Assess for malaria.
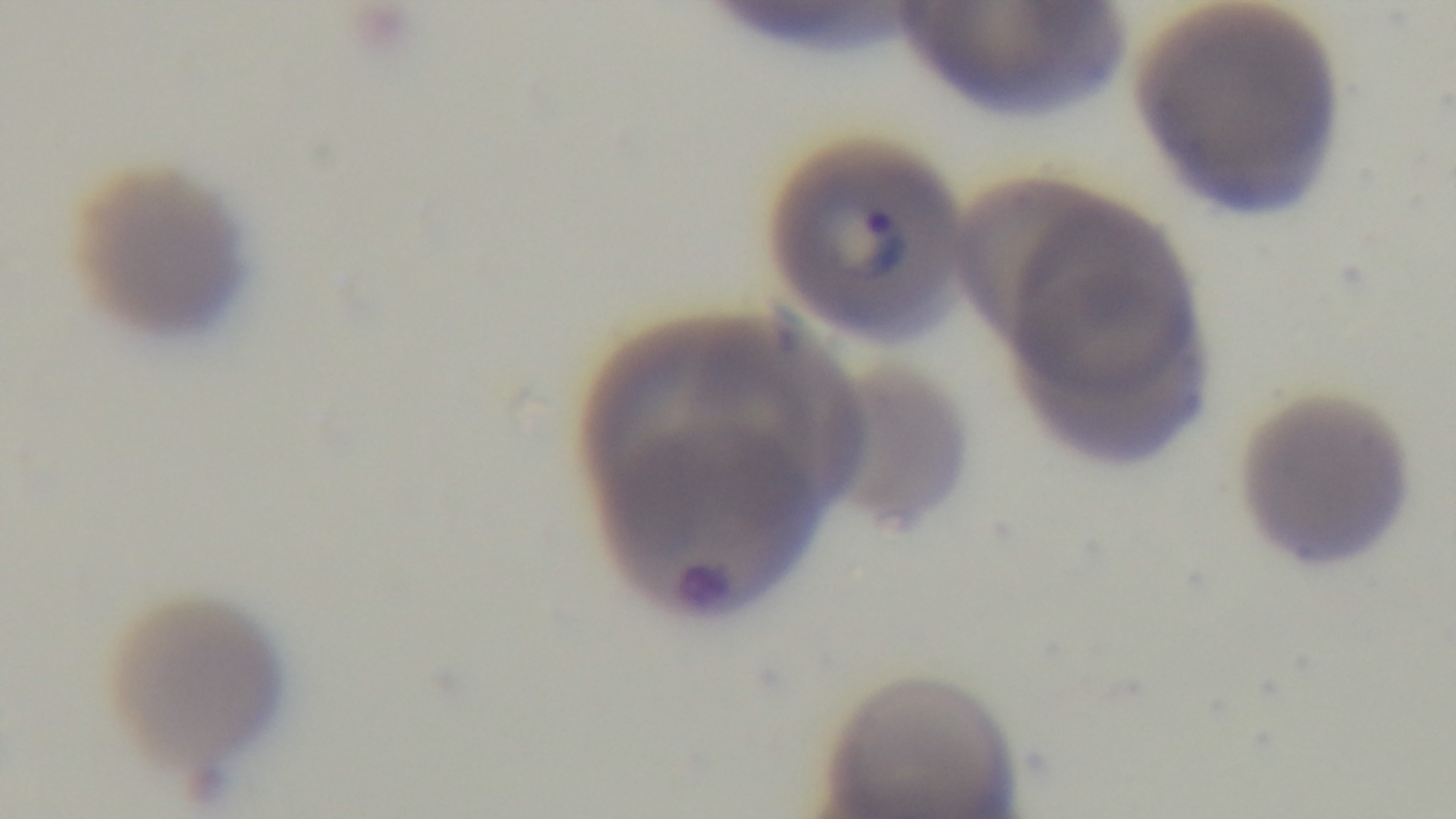
Infected.

{
  "objective": "100x oil immersion",
  "capture": "mounted 4K digital camera",
  "stain": "Giemsa",
  "modality": "light microscopy",
  "preparation": "thin blood film",
  "field_of_view": "single"
}